Assess for malaria.
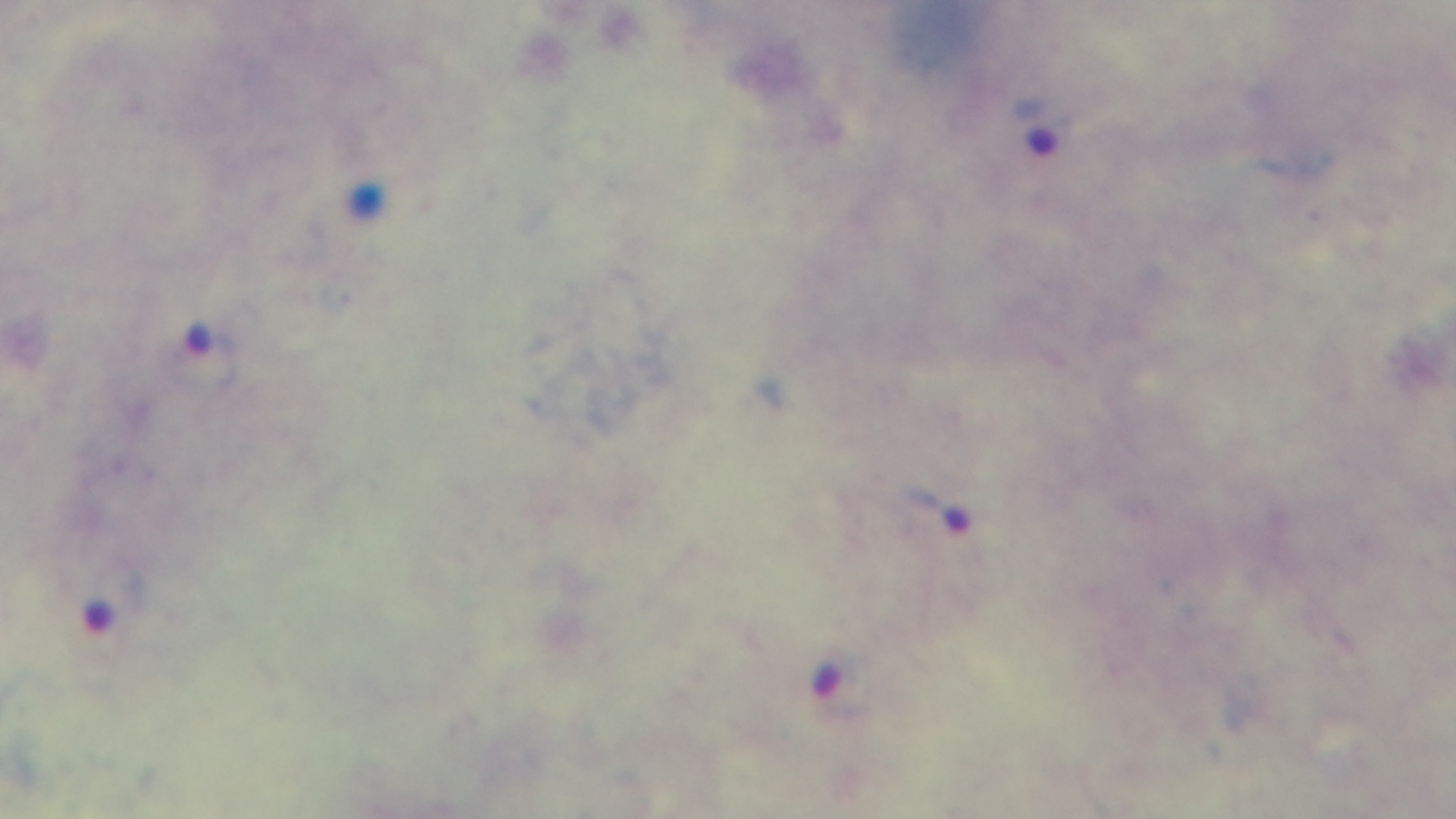
It is infected.

stain: Giemsa
objective: 100x oil immersion
field_of_view: single
capture: mounted 4K digital camera
modality: light microscopy
preparation: thick